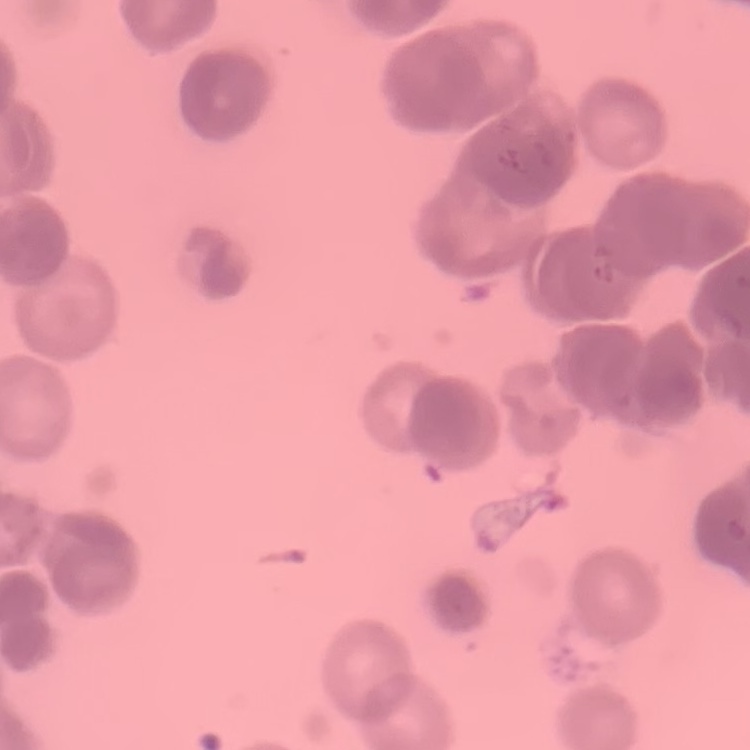

Summary:
  - Erythrocyte morphology: rouleaux formation
  - Preparation: thin blood smear
  - Stain: Field's or Giemsa
  - Image type: square crop of a larger photomicrograph